Identify the cell.
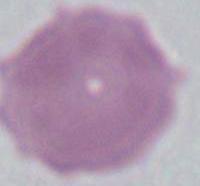

An erythrocyte.

Summary:
  - Modality: photomicrograph
  - Magnification: 1000x